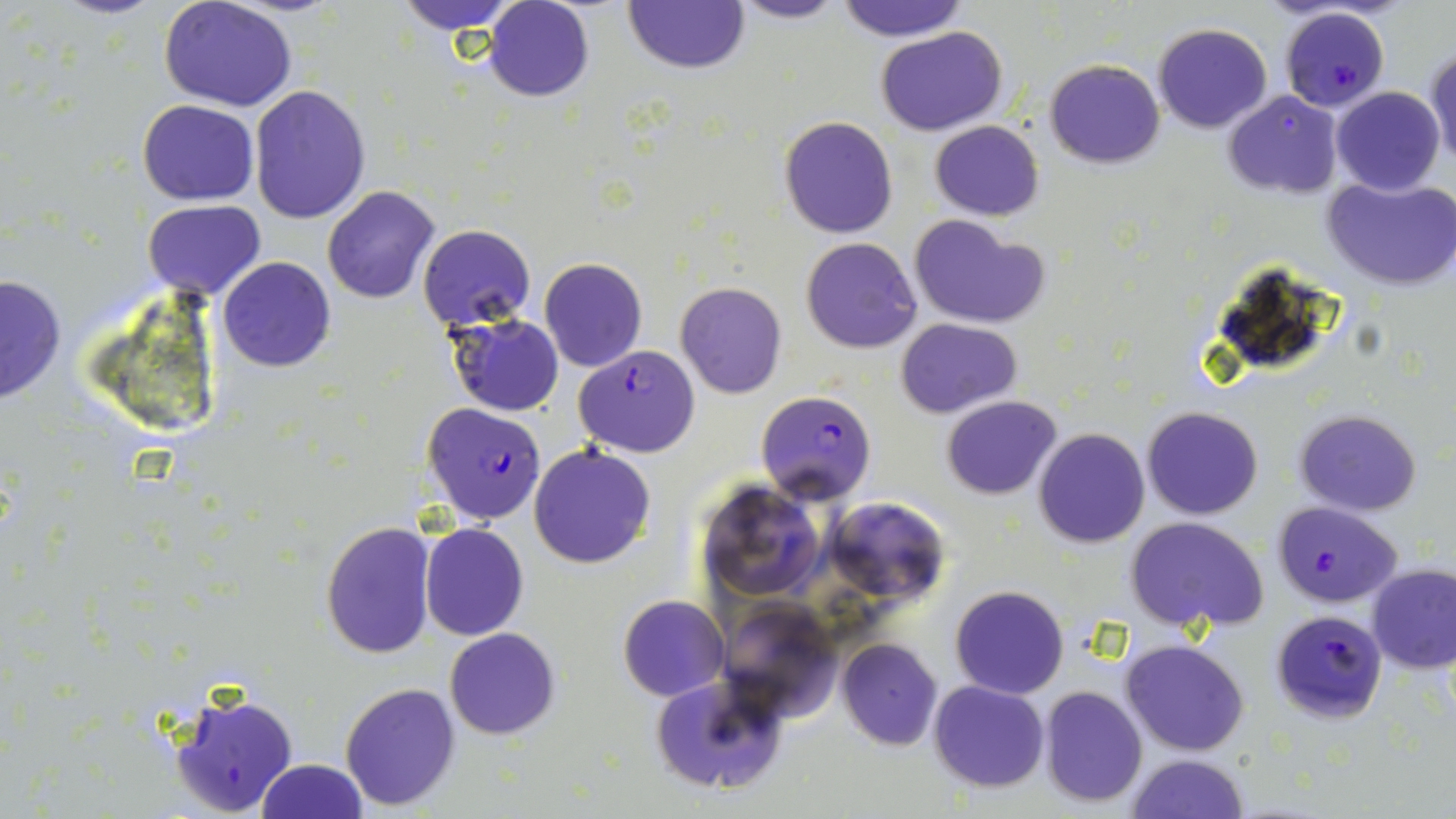

Approximate bounding boxes as named x1/y1/x2/y2 corners in pixels. Uninfected red blood cell locations: (x1=392, y1=0, x2=524, y2=33), (x1=485, y1=0, x2=594, y2=102), (x1=725, y1=0, x2=851, y2=25), (x1=836, y1=0, x2=968, y2=41), (x1=621, y1=1, x2=750, y2=75), (x1=160, y1=2, x2=297, y2=112), (x1=1153, y1=22, x2=1272, y2=133), (x1=876, y1=26, x2=1007, y2=135), (x1=1426, y1=45, x2=1456, y2=175), (x1=1045, y1=59, x2=1164, y2=168), (x1=248, y1=84, x2=371, y2=224), (x1=1333, y1=87, x2=1444, y2=195), (x1=1221, y1=89, x2=1343, y2=199), (x1=137, y1=100, x2=259, y2=205), (x1=780, y1=116, x2=897, y2=238), (x1=929, y1=119, x2=1044, y2=221), (x1=1320, y1=174, x2=1456, y2=292), (x1=322, y1=186, x2=440, y2=304), (x1=144, y1=200, x2=266, y2=302), (x1=909, y1=213, x2=1050, y2=328), (x1=417, y1=224, x2=535, y2=332), (x1=799, y1=237, x2=922, y2=353), (x1=218, y1=256, x2=336, y2=373), (x1=538, y1=258, x2=647, y2=373), (x1=0, y1=274, x2=66, y2=404), (x1=677, y1=281, x2=787, y2=399), (x1=446, y1=313, x2=564, y2=417), (x1=897, y1=318, x2=1022, y2=417), (x1=942, y1=394, x2=1061, y2=498), (x1=1142, y1=406, x2=1263, y2=520), (x1=1294, y1=410, x2=1422, y2=514), (x1=1034, y1=426, x2=1149, y2=548), (x1=527, y1=443, x2=656, y2=569), (x1=696, y1=480, x2=827, y2=605), (x1=820, y1=496, x2=950, y2=606), (x1=1125, y1=515, x2=1270, y2=635), (x1=320, y1=521, x2=434, y2=659), (x1=421, y1=524, x2=529, y2=640), (x1=1367, y1=563, x2=1456, y2=673), (x1=950, y1=585, x2=1070, y2=699), (x1=618, y1=594, x2=729, y2=701), (x1=716, y1=597, x2=843, y2=722), (x1=445, y1=627, x2=561, y2=740), (x1=837, y1=639, x2=943, y2=750), (x1=1120, y1=639, x2=1249, y2=755), (x1=650, y1=673, x2=789, y2=798), (x1=929, y1=680, x2=1050, y2=793), (x1=340, y1=682, x2=460, y2=811), (x1=1040, y1=684, x2=1147, y2=807), (x1=1125, y1=751, x2=1251, y2=819), (x1=256, y1=758, x2=368, y2=819). Plasmodium falciparum-infected red blood cell locations: (x1=1274, y1=7, x2=1394, y2=114), (x1=575, y1=345, x2=698, y2=458), (x1=755, y1=390, x2=877, y2=504), (x1=421, y1=402, x2=547, y2=524), (x1=1271, y1=501, x2=1402, y2=607), (x1=1271, y1=609, x2=1387, y2=721), (x1=168, y1=684, x2=300, y2=817). Slide-level diagnosis: Plasmodium falciparum. Thin blood smear. Light microscopy. May-Grünwald-Giemsa stain. 1000x magnification. Image is 1456×819 pixels. One field of a larger specimen.